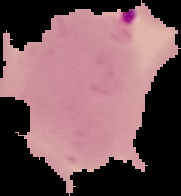
Summary:
  - Image type: segmented cell region with the area outside set to black
  - Malaria status: parasitized
  - Preparation: thin blood smear
  - Image size: 181×196 pixels